Comment on the morphology of the red blood cells.
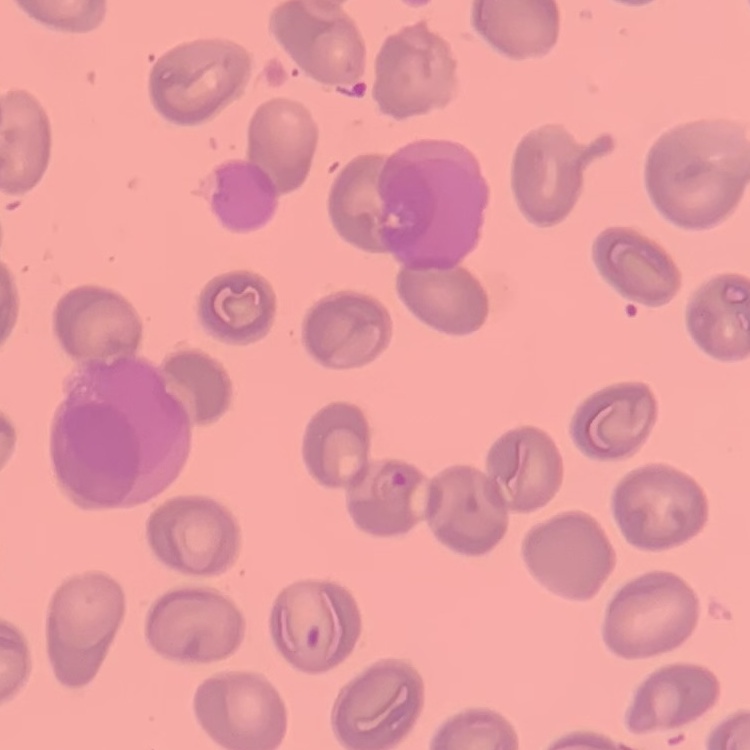
No rouleaux formation.

stain: Field's or Giemsa
image_type: square crop of a larger photomicrograph
preparation: thin blood film